Outline each blood parasite and name the species.
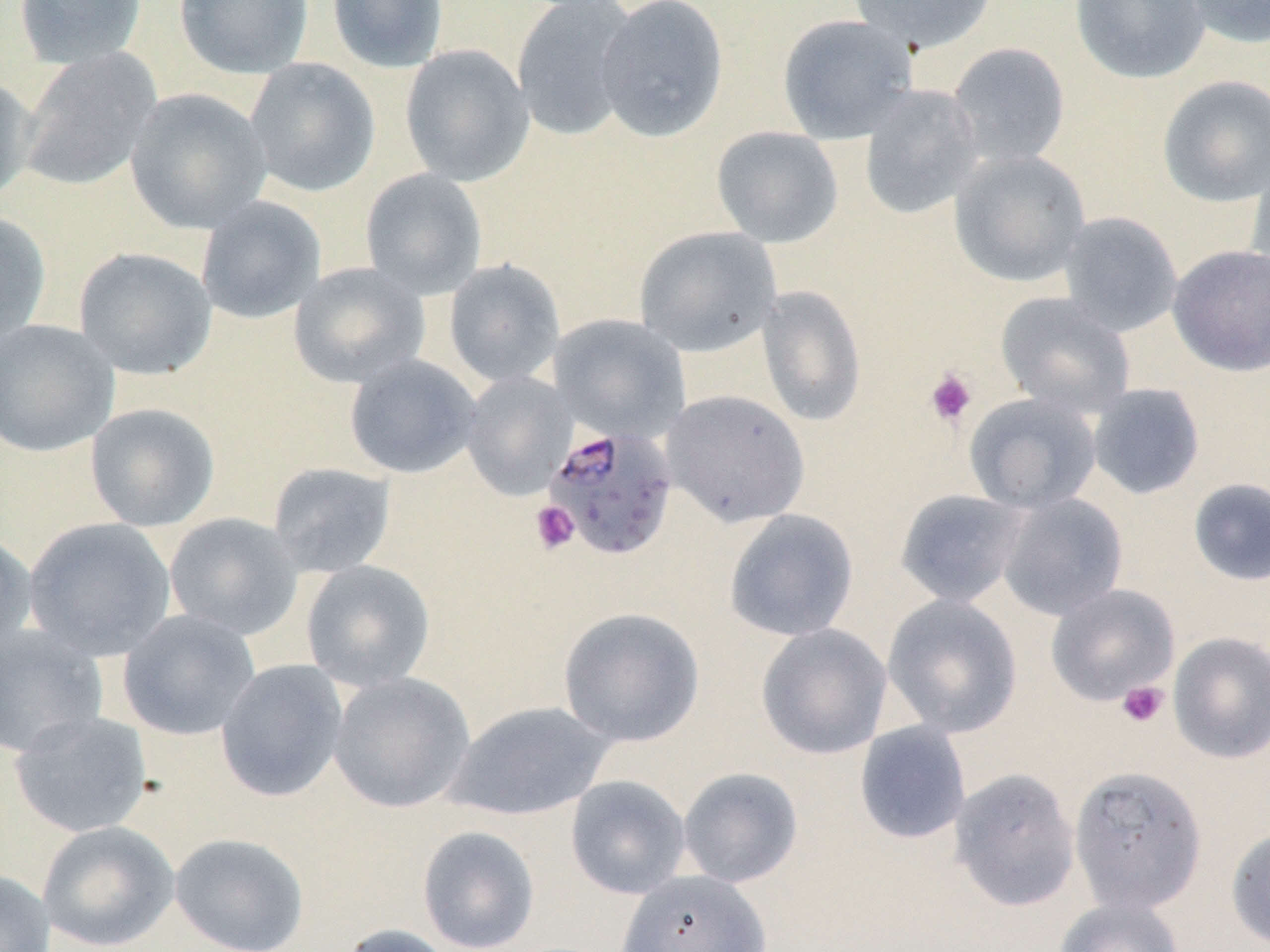

Approximate bounding boxes as named x1/y1/x2/y2 corners in pixels.
Plasmodium falciparum-infected red blood cells: (x1=543, y1=424, x2=679, y2=561).
No Plasmodium ovale, Plasmodium malariae, Plasmodium vivax, Babesia divergens, or Trypanosoma brucei observed.

slide_level_diagnosis: Plasmodium falciparum
preparation: thin blood smear
image_size: 1270×952 pixels
magnification: 1000x
uninfected_red_blood_cell_locations: 'approximate bounding boxes as named x1/y1/x2/y2 corners in pixels: (x1=12, y1=0, x2=149, y2=69), (x1=173, y1=0, x2=314, y2=79), (x1=326, y1=0, x2=449, y2=73), (x1=511, y1=0, x2=640, y2=141), (x1=595, y1=0, x2=729, y2=142), (x1=848, y1=0, x2=998, y2=53), (x1=1070, y1=0, x2=1210, y2=84), (x1=1179, y1=0, x2=1270, y2=48), (x1=776, y1=14, x2=918, y2=144), (x1=948, y1=42, x2=1071, y2=169), (x1=399, y1=44, x2=534, y2=186), (x1=17, y1=48, x2=162, y2=192), (x1=244, y1=57, x2=381, y2=198), (x1=0, y1=73, x2=37, y2=205), (x1=1157, y1=74, x2=1270, y2=207), (x1=858, y1=84, x2=984, y2=220), (x1=125, y1=88, x2=272, y2=234), (x1=711, y1=126, x2=844, y2=248), (x1=949, y1=150, x2=1091, y2=287), (x1=1245, y1=153, x2=1270, y2=290), (x1=360, y1=168, x2=488, y2=299), (x1=195, y1=196, x2=326, y2=324), (x1=1056, y1=210, x2=1183, y2=336), (x1=0, y1=211, x2=51, y2=347), (x1=634, y1=225, x2=782, y2=358), (x1=1167, y1=243, x2=1270, y2=377), (x1=73, y1=246, x2=218, y2=380), (x1=444, y1=258, x2=565, y2=388), (x1=288, y1=262, x2=430, y2=389), (x1=757, y1=286, x2=866, y2=426), (x1=995, y1=292, x2=1136, y2=418), (x1=549, y1=314, x2=690, y2=442), (x1=0, y1=318, x2=120, y2=458), (x1=344, y1=354, x2=482, y2=479), (x1=461, y1=371, x2=576, y2=501), (x1=1087, y1=383, x2=1206, y2=500), (x1=661, y1=389, x2=810, y2=527), (x1=964, y1=393, x2=1102, y2=514), (x1=84, y1=402, x2=221, y2=532), (x1=266, y1=461, x2=397, y2=578), (x1=1188, y1=477, x2=1270, y2=587), (x1=894, y1=488, x2=1030, y2=608), (x1=996, y1=492, x2=1129, y2=621), (x1=723, y1=509, x2=859, y2=642), (x1=163, y1=512, x2=304, y2=641), (x1=23, y1=517, x2=177, y2=661), (x1=0, y1=528, x2=37, y2=658), (x1=300, y1=560, x2=436, y2=692), (x1=1045, y1=583, x2=1181, y2=706), (x1=882, y1=593, x2=1023, y2=738), (x1=558, y1=606, x2=705, y2=747), (x1=117, y1=609, x2=261, y2=741), (x1=755, y1=623, x2=892, y2=760), (x1=0, y1=624, x2=109, y2=759), (x1=1167, y1=631, x2=1270, y2=764), (x1=215, y1=659, x2=349, y2=803), (x1=328, y1=672, x2=475, y2=813), (x1=444, y1=700, x2=615, y2=821), (x1=8, y1=710, x2=154, y2=838), (x1=853, y1=721, x2=971, y2=845), (x1=1068, y1=765, x2=1208, y2=914), (x1=678, y1=767, x2=803, y2=888), (x1=949, y1=767, x2=1080, y2=911), (x1=565, y1=775, x2=691, y2=899), (x1=37, y1=820, x2=179, y2=951), (x1=416, y1=825, x2=540, y2=952), (x1=1225, y1=825, x2=1270, y2=950), (x1=169, y1=832, x2=310, y2=952), (x1=0, y1=868, x2=56, y2=952), (x1=615, y1=870, x2=772, y2=952), (x1=1054, y1=896, x2=1185, y2=952), (x1=337, y1=923, x2=459, y2=952)'
platelet_locations: 'approximate bounding boxes as named x1/y1/x2/y2 corners in pixels: (x1=924, y1=367, x2=978, y2=427), (x1=530, y1=500, x2=580, y2=555), (x1=1117, y1=680, x2=1169, y2=728)'
modality: optical microscopy
stain: May-Grünwald-Giemsa
field_of_view: single